Outline each Plasmodium malariae-infected red blood cell.
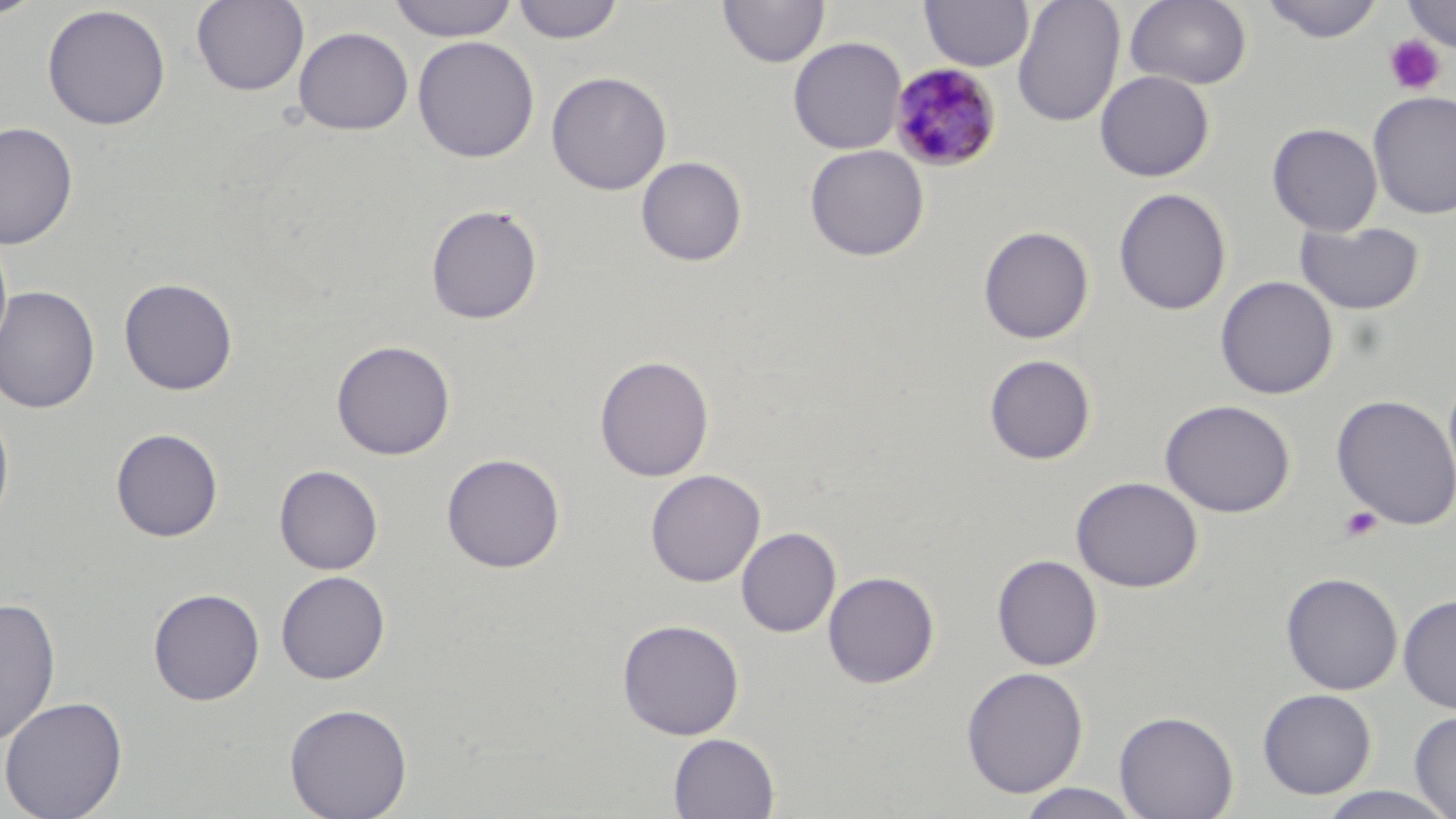

Approximate bounding boxes as named x1/y1/x2/y2 corners in pixels.
Plasmodium malariae-infected red blood cells: (x1=887, y1=62, x2=1002, y2=172).

Uninfected red blood cell locations: (x1=0, y1=0, x2=45, y2=21), (x1=191, y1=0, x2=309, y2=97), (x1=387, y1=0, x2=519, y2=42), (x1=511, y1=0, x2=624, y2=44), (x1=717, y1=0, x2=829, y2=68), (x1=919, y1=0, x2=1034, y2=71), (x1=1012, y1=0, x2=1125, y2=127), (x1=1125, y1=0, x2=1252, y2=90), (x1=1261, y1=0, x2=1384, y2=44), (x1=1401, y1=0, x2=1456, y2=53), (x1=41, y1=4, x2=171, y2=130), (x1=293, y1=26, x2=414, y2=136), (x1=412, y1=35, x2=539, y2=163), (x1=788, y1=37, x2=907, y2=154), (x1=1094, y1=70, x2=1215, y2=182), (x1=546, y1=71, x2=672, y2=196), (x1=1367, y1=90, x2=1456, y2=220), (x1=0, y1=122, x2=78, y2=250), (x1=1267, y1=122, x2=1383, y2=236), (x1=805, y1=144, x2=929, y2=262), (x1=636, y1=156, x2=748, y2=266), (x1=1113, y1=187, x2=1231, y2=315), (x1=425, y1=204, x2=543, y2=325), (x1=1294, y1=220, x2=1425, y2=315), (x1=978, y1=225, x2=1094, y2=344), (x1=1215, y1=275, x2=1338, y2=400), (x1=118, y1=277, x2=239, y2=396), (x1=0, y1=285, x2=100, y2=414), (x1=331, y1=339, x2=456, y2=460), (x1=984, y1=353, x2=1096, y2=465), (x1=594, y1=354, x2=714, y2=482), (x1=1331, y1=394, x2=1456, y2=531), (x1=1160, y1=399, x2=1295, y2=518), (x1=0, y1=402, x2=15, y2=538), (x1=110, y1=428, x2=224, y2=542), (x1=442, y1=453, x2=565, y2=573), (x1=275, y1=464, x2=383, y2=575), (x1=645, y1=469, x2=766, y2=587), (x1=1071, y1=476, x2=1202, y2=593), (x1=736, y1=527, x2=840, y2=637), (x1=991, y1=554, x2=1103, y2=671), (x1=276, y1=570, x2=390, y2=684), (x1=822, y1=570, x2=940, y2=688), (x1=1280, y1=572, x2=1403, y2=695), (x1=148, y1=587, x2=265, y2=705), (x1=1398, y1=593, x2=1456, y2=715), (x1=0, y1=595, x2=61, y2=747), (x1=617, y1=618, x2=745, y2=740), (x1=960, y1=666, x2=1088, y2=798), (x1=1257, y1=688, x2=1377, y2=799), (x1=0, y1=695, x2=128, y2=818), (x1=284, y1=702, x2=413, y2=819), (x1=1114, y1=710, x2=1238, y2=819), (x1=1409, y1=710, x2=1456, y2=818), (x1=668, y1=733, x2=780, y2=818), (x1=1014, y1=783, x2=1145, y2=818), (x1=1314, y1=786, x2=1456, y2=819). Platelet locations: (x1=1401, y1=1, x2=1456, y2=55), (x1=1383, y1=33, x2=1447, y2=96), (x1=1339, y1=506, x2=1383, y2=543). Slide-level diagnosis: Plasmodium malariae. Light microscopy. One field of a larger specimen. Thin blood smear. Image is 1456×819 pixels. Captured at 1000x magnification. May-Grünwald-Giemsa-stained preparation.